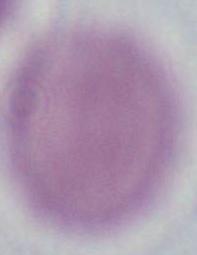
Summary:
  - Identification: erythrocyte
  - Modality: micrograph
  - Magnification: 1000x